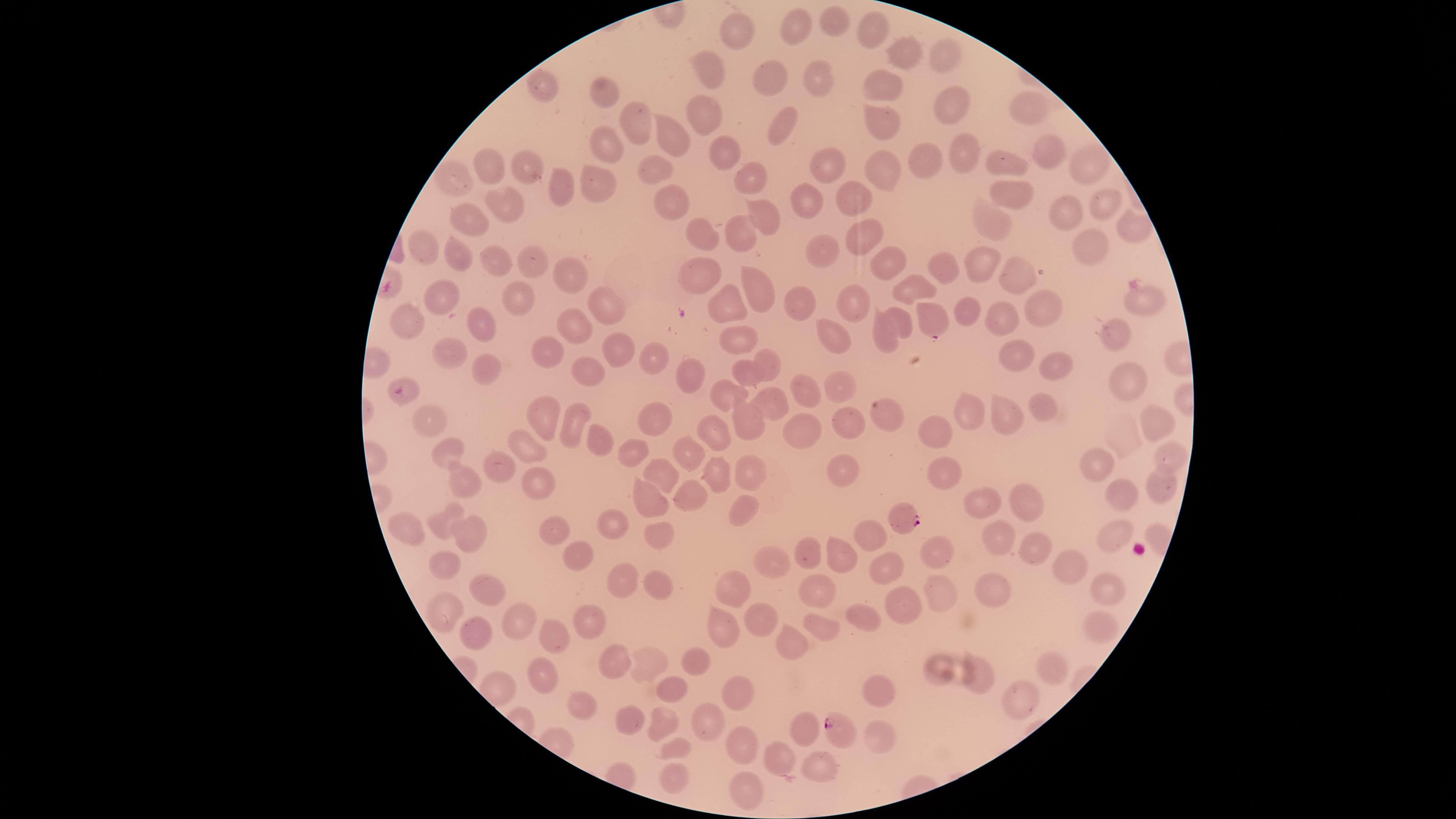

Approximate marker points as {x, y} in pixels.
Summary:
  - Uninfected red blood cells: {799, 23}, {833, 23}, {866, 26}, {734, 36}, {906, 49}, {944, 53}, {774, 71}, {707, 75}, {815, 75}, {874, 80}, {549, 86}, {610, 92}, {954, 101}, {1029, 109}, {703, 111}, {781, 115}, {878, 117}, {635, 125}, {666, 132}, {607, 141}, {722, 149}, {1045, 149}, {959, 152}, {1010, 157}, {920, 159}, {823, 160}, {495, 164}, {659, 164}, {877, 165}, {1086, 165}, {527, 170}, {455, 172}, {749, 172}, {601, 181}, {564, 182}, {1009, 188}, {805, 190}, {854, 193}, {503, 199}, {673, 199}, {1104, 203}, {764, 209}, {1062, 212}, {469, 214}, {990, 219}, {1130, 223}, {867, 230}, {703, 233}, {739, 233}, {1093, 239}, {425, 245}, {819, 251}, {459, 253}, {493, 255}, {525, 258}, {887, 258}, {989, 258}, {940, 263}, {1023, 267}, {700, 270}, {563, 273}, {756, 285}, {905, 287}, {443, 290}, {518, 297}, {1141, 297}, {853, 298}, {729, 299}, {803, 302}, {606, 307}, {1040, 307}, {966, 310}, {413, 316}, {901, 316}, {1003, 320}, {482, 322}, {568, 325}, {1116, 331}, {737, 333}, {833, 333}, {885, 336}, {445, 342}, {616, 346}, {548, 350}, {1019, 351}, {660, 352}, {766, 363}, {1058, 364}, {488, 366}, {592, 366}, {743, 371}, {688, 372}, {1122, 375}, {838, 385}, {804, 386}, {727, 390}, {768, 396}, {972, 402}, {1040, 403}, {653, 411}, {889, 412}, {1006, 413}, {1152, 416}, {543, 419}, {747, 420}, {842, 420}, {428, 422}, {572, 422}, {712, 423}, {801, 426}, {936, 429}, {600, 437}, {520, 444}, {630, 452}, {453, 454}, {1170, 455}, {692, 458}, {1102, 459}, {843, 472}, {499, 473}, {716, 476}, {744, 477}, {941, 477}, {462, 479}, {661, 479}, {542, 481}, {1158, 484}, {688, 490}, {1118, 492}, {980, 498}, {648, 502}, {1026, 502}, {739, 506}, {447, 518}, {611, 526}, {471, 533}, {660, 533}, {1110, 534}, {400, 535}, {999, 536}, {874, 537}, {557, 538}, {1032, 547}, {839, 548}, {932, 548}, {810, 549}, {580, 558}, {773, 558}, {1072, 561}, {444, 564}, {890, 564}, {658, 578}, {621, 581}, {1110, 582}, {816, 585}, {939, 587}, {741, 589}, {493, 590}, {982, 590}, {901, 597}, {448, 609}, {523, 612}, {858, 615}, {768, 619}, {821, 624}, {582, 625}, {723, 626}, {1101, 626}, {481, 629}, {792, 637}, {552, 640}, {612, 658}, {696, 659}, {647, 660}, {1050, 662}, {937, 668}, {974, 672}, {543, 680}, {668, 690}, {872, 690}, {736, 693}, {1012, 698}, {579, 703}, {664, 720}, {621, 722}, {708, 724}, {803, 725}, {878, 736}, {743, 741}, {673, 748}, {777, 757}, {813, 766}, {672, 777}, {749, 792}
  - Parasitized red blood cells: {931, 320}, {404, 392}, {904, 518}, {836, 730}
  - Preparation: thin blood smear
  - Field of view: single
  - Presence: malaria parasites detected
  - Image size: 1456×819 pixels
  - Stain: Giemsa
  - Capture: smartphone photograph through the microscope eyepiece
  - Species: Plasmodium falciparum
  - Visible region: circular